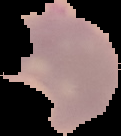

{
  "preparation": "thin blood film",
  "result": "Plasmodium parasites identified",
  "image_size": "121×136 pixels",
  "image_type": "segmented cell region with the area outside set to black"
}